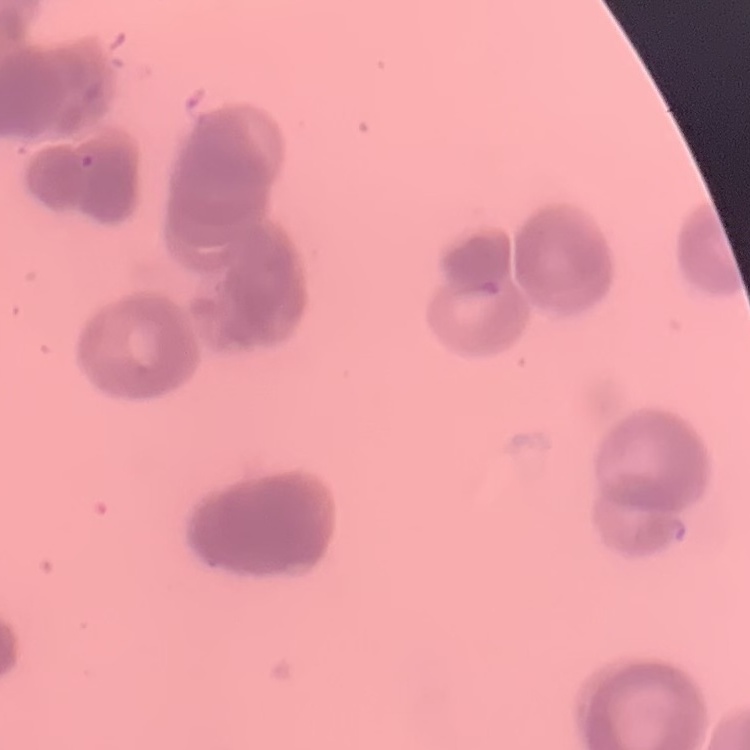

erythrocyte_morphology: rouleaux formation
preparation: thin blood smear
stain: Field's or Giemsa
image_type: one tile cut from a larger photomicrograph